Identify the preparation type.
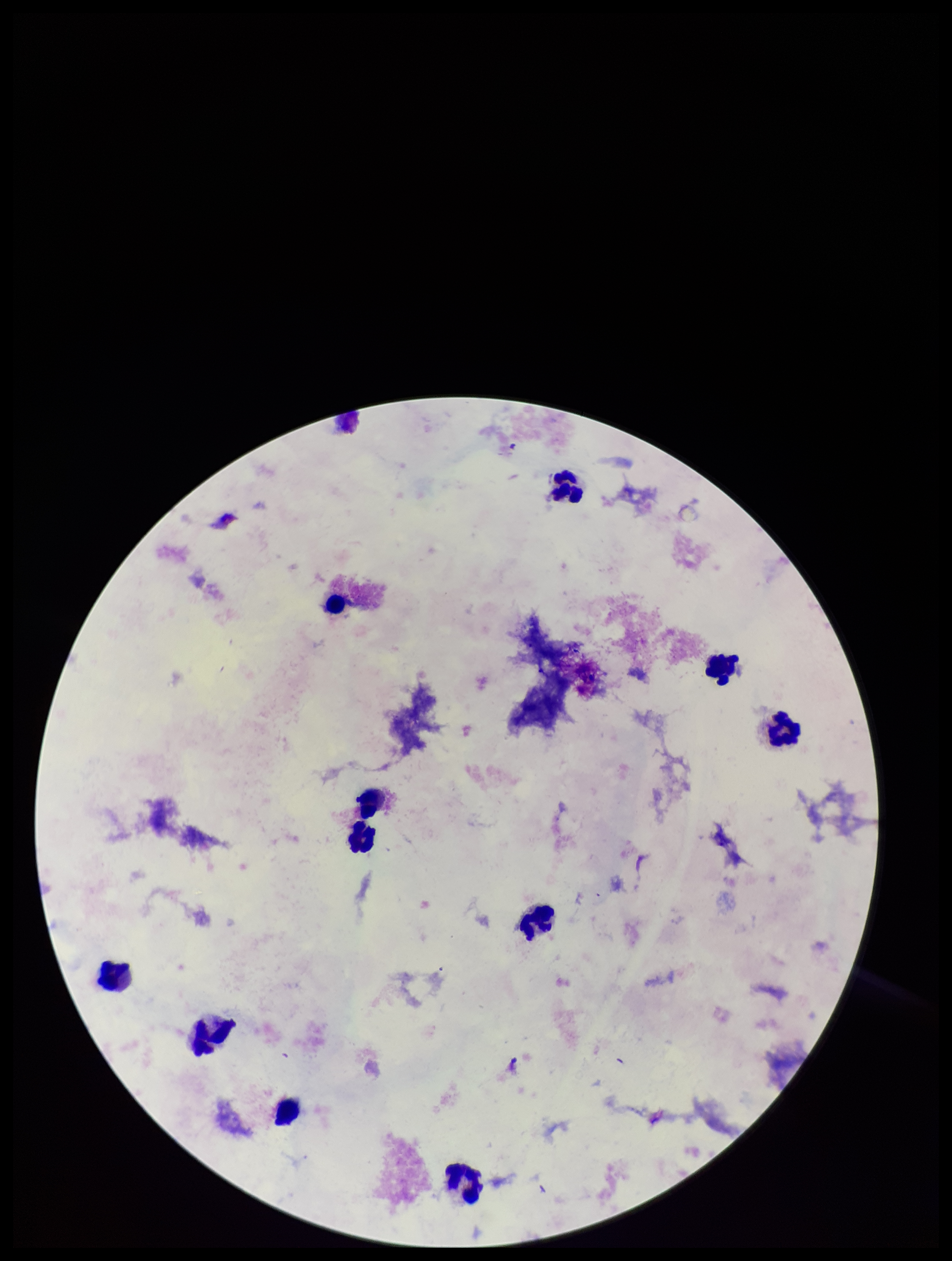
It is a thick blood smear.

Patient malaria status: negative. Single field of view. Parasite count: 0. Image is 952×1261 pixels. Leukocyte count: 11. Plasmodium parasites: none detected. Stained with Giemsa. Photographed through the microscope eyepiece with a smartphone camera.